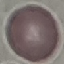

malaria_status: uninfected
image_type: automatically extracted cell patch, resized to 64 × 64 pixels
preparation: thin blood smear
capture: smartphone camera at the microscope eyepiece
stain: Giemsa